Locate every malaria parasite by life-cycle stage, and every leukocyte.
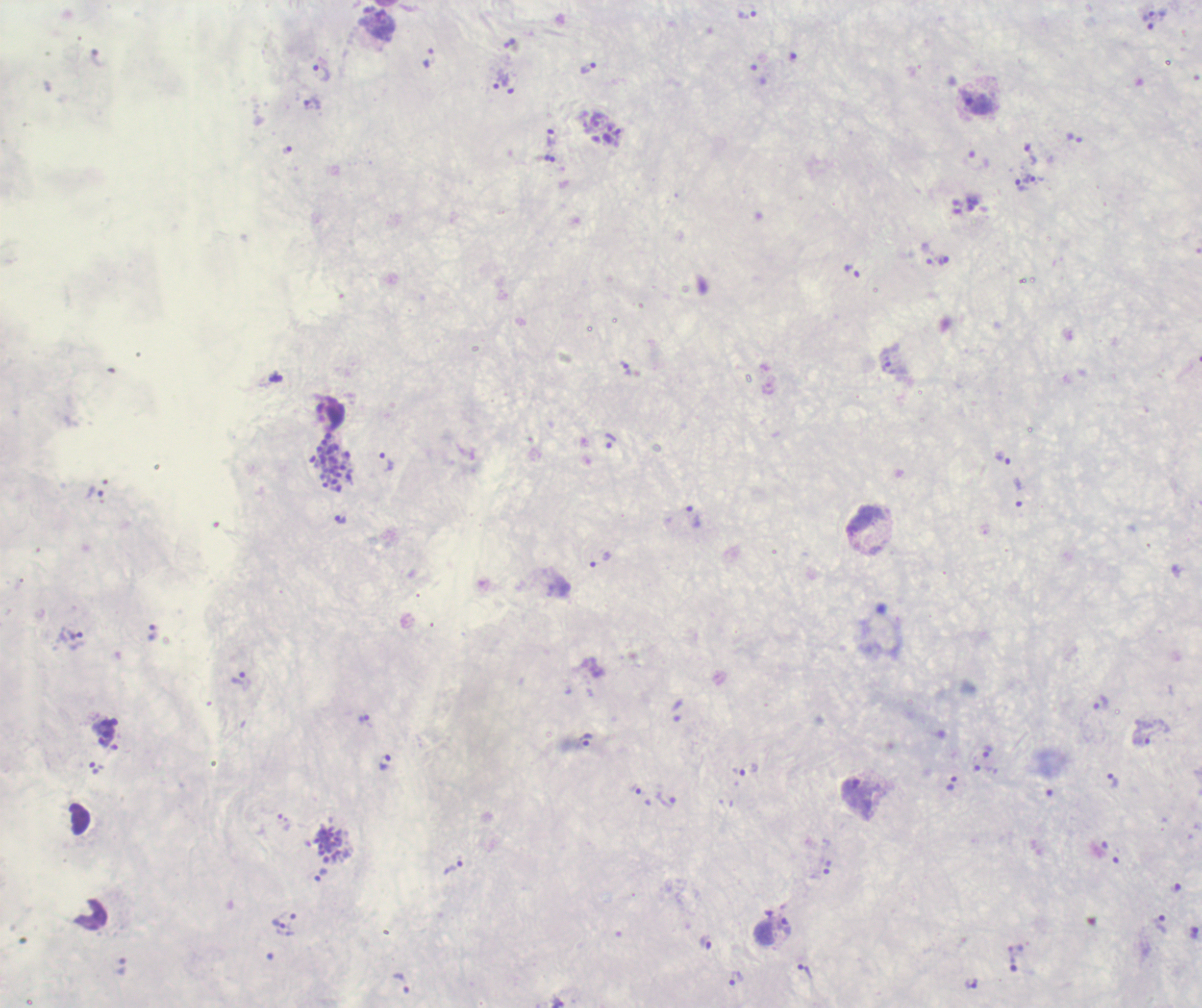
Approximate object centers, in pixels from the top-left corner.
Trophozoites: (x=748, y=14), (x=1148, y=16), (x=430, y=58), (x=587, y=68), (x=321, y=73), (x=502, y=80), (x=979, y=104), (x=312, y=105), (x=598, y=120), (x=552, y=137), (x=1030, y=155), (x=1030, y=179), (x=1022, y=185), (x=943, y=260), (x=890, y=367), (x=625, y=368), (x=610, y=440), (x=1002, y=458), (x=387, y=462), (x=1018, y=493), (x=693, y=516), (x=340, y=519), (x=865, y=519), (x=600, y=559), (x=153, y=633), (x=239, y=679), (x=1100, y=703), (x=678, y=711), (x=363, y=718), (x=586, y=739), (x=1140, y=740), (x=988, y=751), (x=385, y=762), (x=745, y=770), (x=1112, y=780), (x=952, y=783), (x=634, y=788), (x=856, y=794), (x=665, y=800), (x=453, y=867), (x=827, y=868), (x=321, y=874), (x=279, y=923), (x=1160, y=924), (x=784, y=927), (x=705, y=940), (x=1013, y=959), (x=805, y=971), (x=735, y=979), (x=401, y=983), (x=971, y=984).
Schizonts: (x=331, y=462), (x=329, y=846).
No gametocyte forms observed.
No leukocytes visible.

Summary:
  - Context: previously used in a real diagnosis
  - Magnification: 100x
  - Stain: Romanowsky
  - Field of view: one from this slide
  - Image size: 1202×1008 pixels
  - Preparation: thick smear of blood
  - Background quality: poor
  - Coloration quality: bad